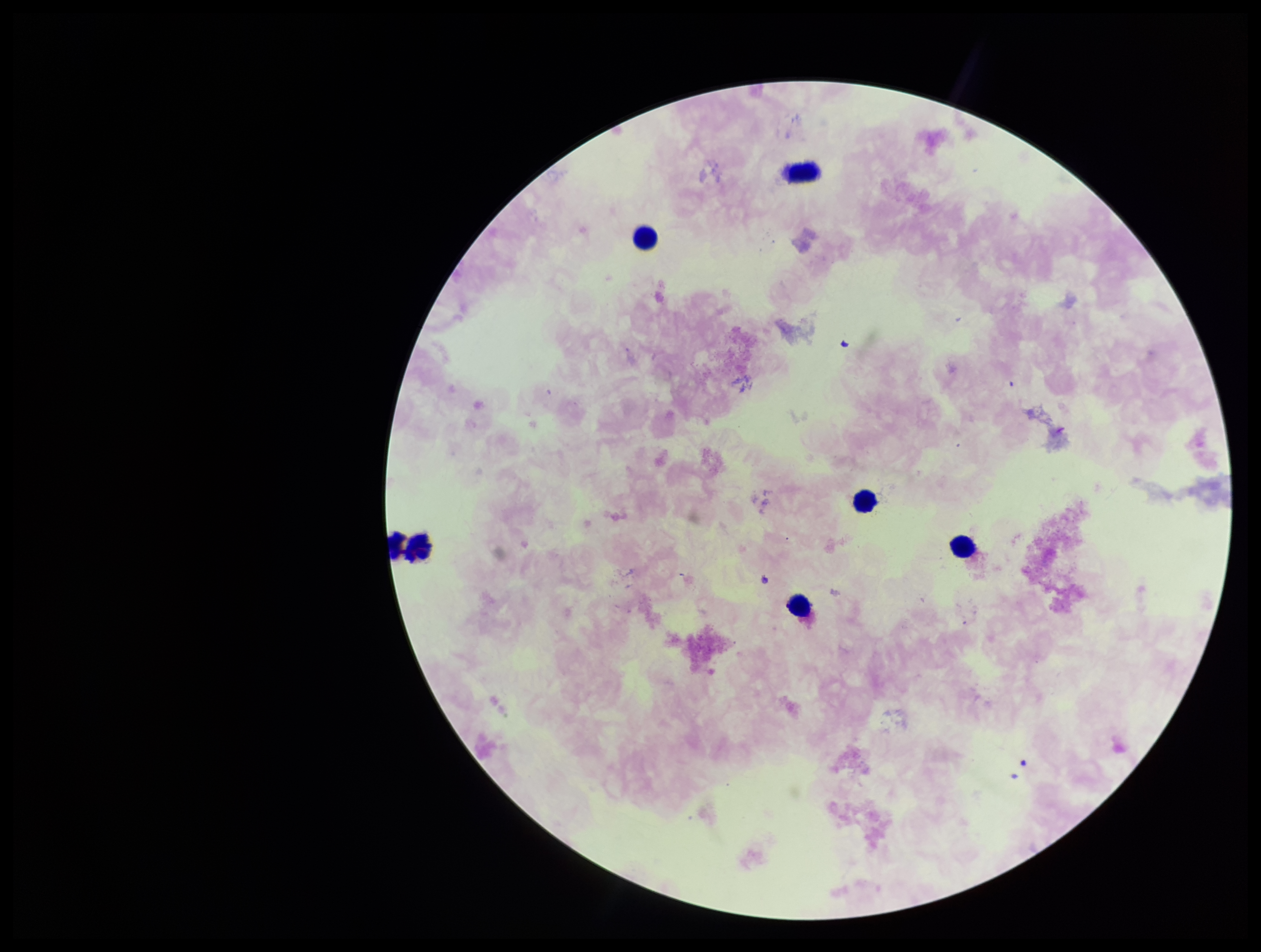 Image is 1261×952 pixels. Patient malaria status: negative. Leukocyte count: 5. One field from this slide. Parasite count: 0. Stained with Giemsa. Preparation: thick smear. Photographed through the microscope eyepiece with a smartphone camera. Plasmodium parasites: none detected.